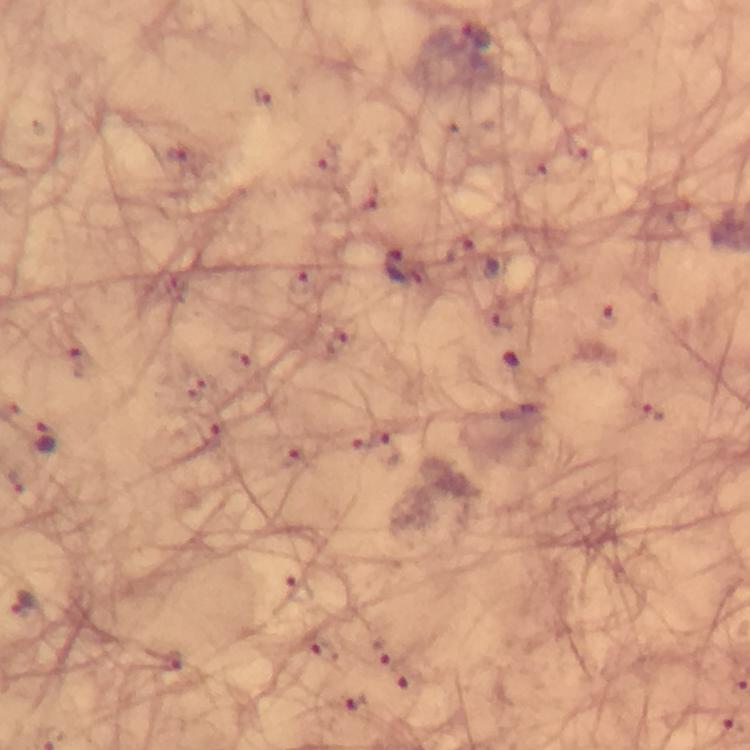 Approximate centers as {x, y} in pixels. Malaria parasite locations: {475, 36}, {326, 159}, {368, 200}, {460, 251}, {393, 266}, {300, 279}, {609, 316}, {336, 342}, {653, 411}, {46, 439}, {387, 448}, {22, 602}, {317, 646}, {379, 651}, {169, 661}, {410, 681}, {355, 701}. 100x magnification. Cropped region of a single field of view. Thick blood film. Giemsa-stained preparation. Image is 750×750 pixels. Photographed with a smartphone mounted on the microscope. Immersion oil applied. From a malaria diagnostic workup.